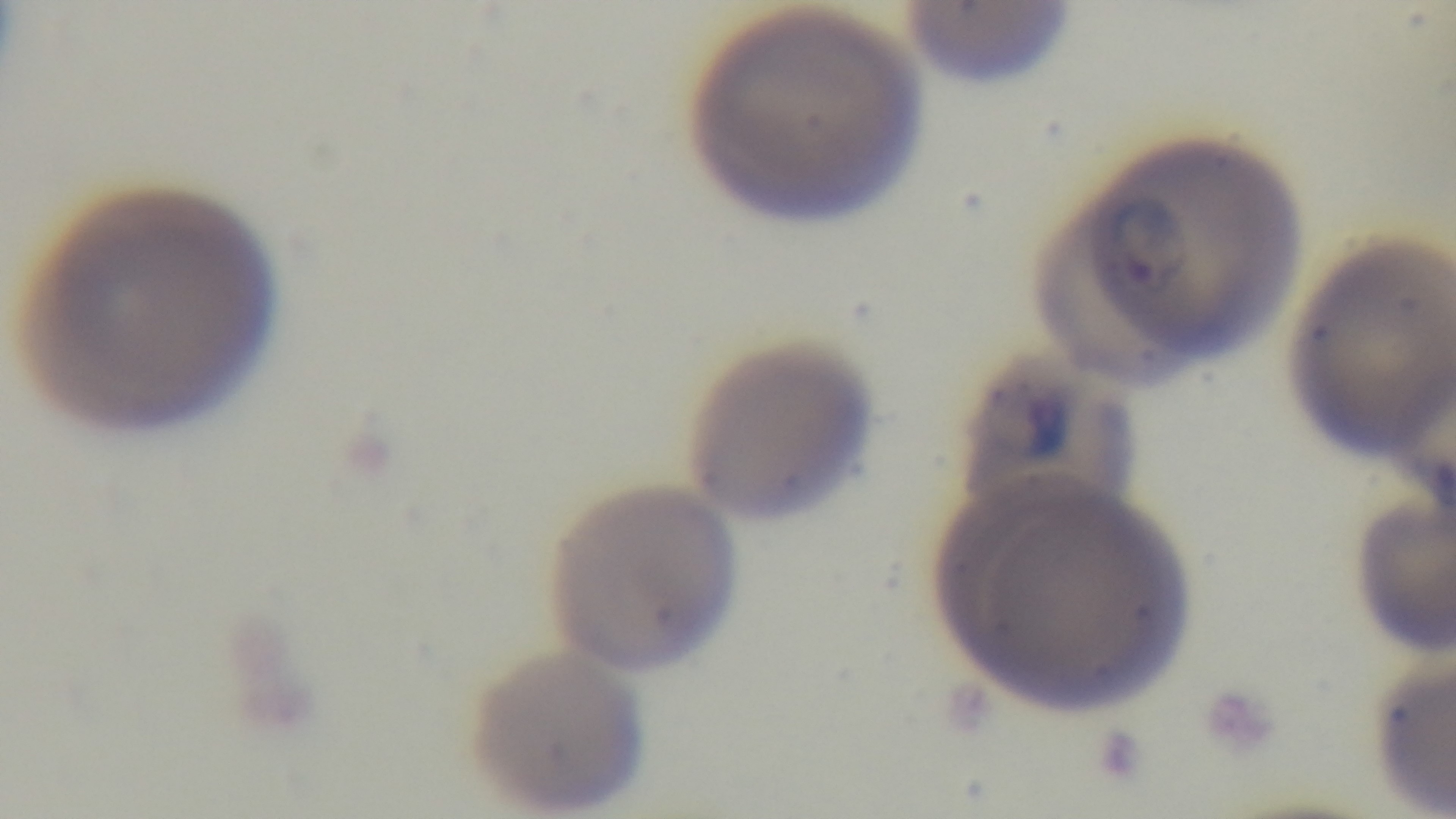
Giemsa-stained. Captured with a mounted 4K digital camera. Light microscopy. One field from the slide. Preparation: thin. 100x oil-immersion objective. Malaria status: infected.